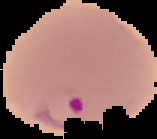

image size = 157×139 pixels
image type = segmented cell region on a black background
malaria status = parasitized
preparation = thin blood smear